State which parasite is depicted.
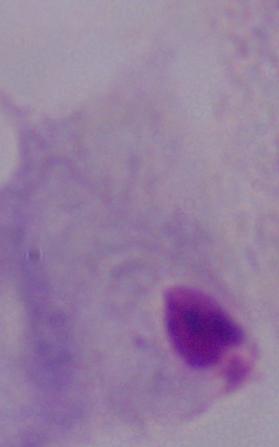
A trichomonad.

Summary:
  - Magnification: 1000x
  - Modality: micrograph